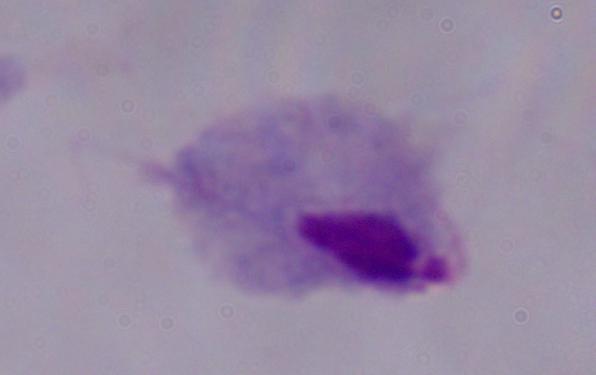
{
  "identification": "trichomonad",
  "modality": "photomicrograph",
  "magnification": "1000x"
}